Give the position of each P. falciparum parasite with its life-cycle stage, each leukocyte, and any debris.
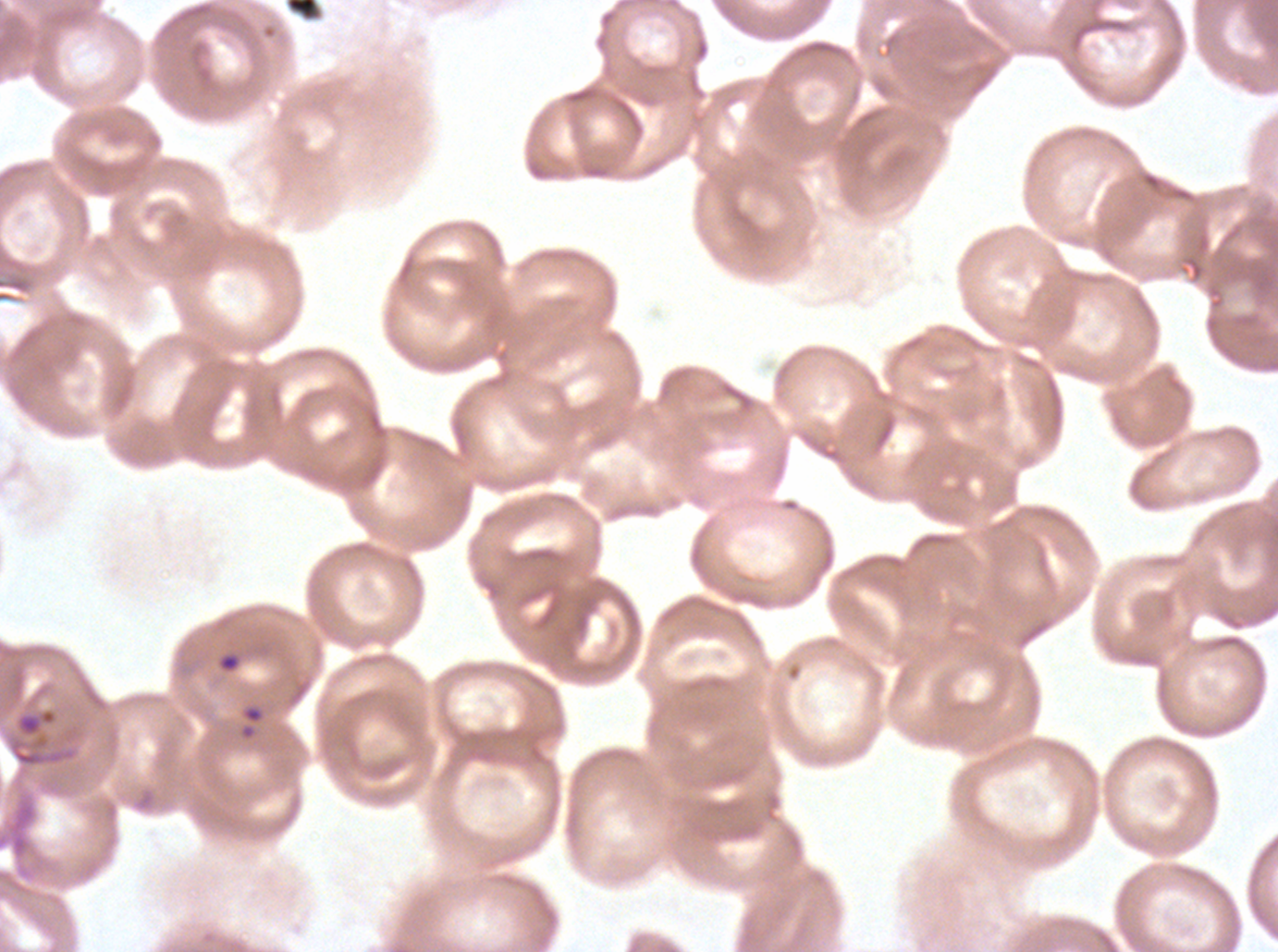
Approximate bounding boxes as [x1, y1, x2, y2] in pixels.
Debris: [216, 653, 241, 673], [8, 707, 78, 768].
No rings, late-ring/early-trophozoite forms, mid trophozoites, late trophozoites, early schizonts, late schizonts, segmenters, gametocytes, or leukocytes observed.

Image is 1278×952 pixels. Thin blood smear. P. falciparum cultured ex vivo for 24 to 48 hours, from a patient in The Gambia. One sub-image of a larger composite. Giemsa-stained preparation.